Identify the blood parasite species.
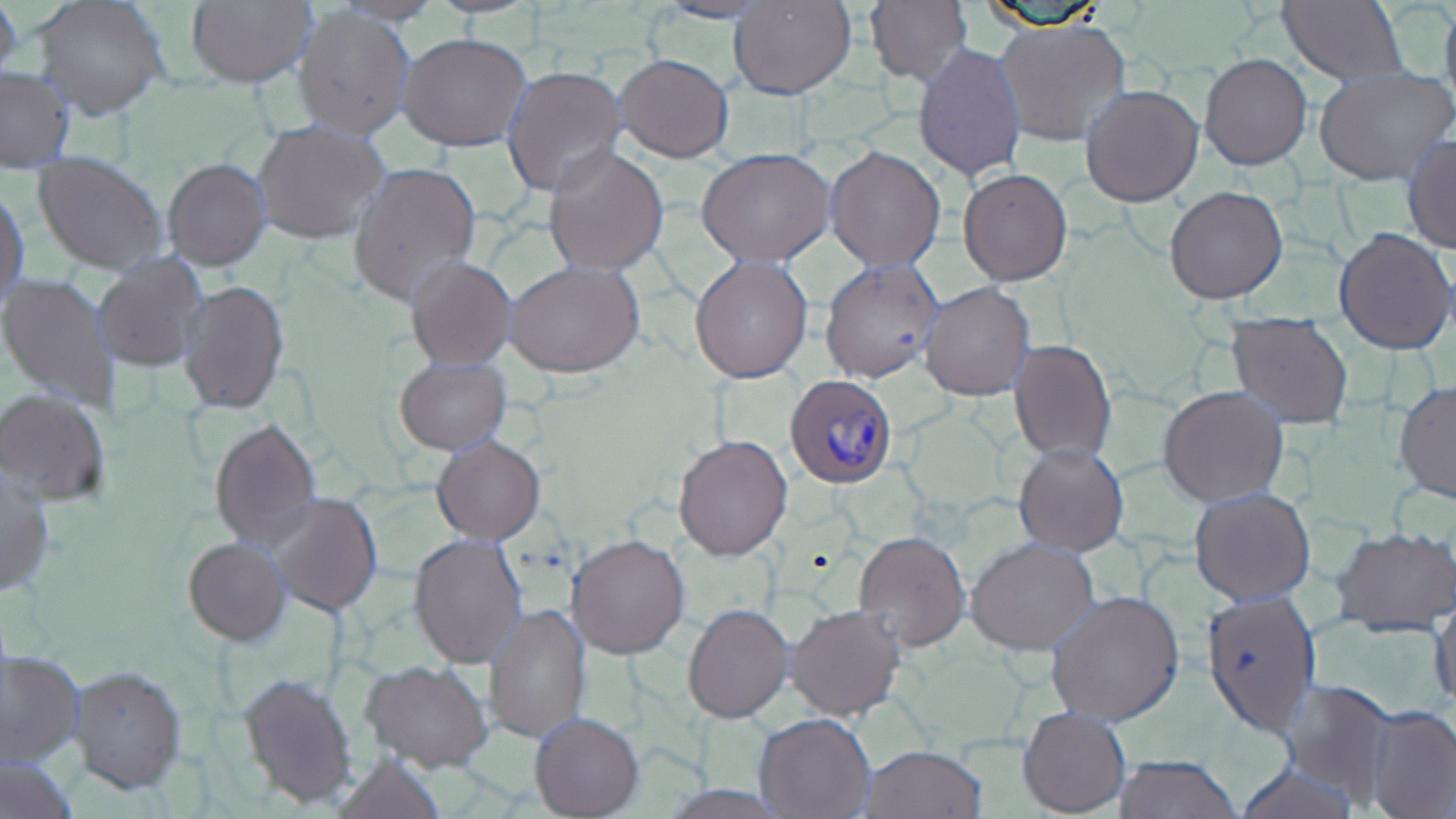
Plasmodium ovale.

Approximate bounding boxes as named x1/y1/x2/y2 corners in pixels. Plasmodium ovale-infected red blood cell locations: (x1=785, y1=373, x2=899, y2=486). Uninfected red blood cell locations: (x1=0, y1=0, x2=23, y2=85), (x1=33, y1=0, x2=170, y2=120), (x1=185, y1=0, x2=314, y2=89), (x1=729, y1=0, x2=856, y2=99), (x1=866, y1=0, x2=973, y2=88), (x1=1278, y1=0, x2=1407, y2=87), (x1=1439, y1=0, x2=1456, y2=117), (x1=651, y1=1, x2=779, y2=23), (x1=293, y1=5, x2=415, y2=139), (x1=994, y1=18, x2=1131, y2=146), (x1=398, y1=32, x2=533, y2=152), (x1=913, y1=42, x2=1027, y2=183), (x1=615, y1=53, x2=733, y2=163), (x1=1198, y1=53, x2=1312, y2=170), (x1=501, y1=66, x2=628, y2=198), (x1=1314, y1=67, x2=1454, y2=185), (x1=0, y1=68, x2=73, y2=173), (x1=1081, y1=84, x2=1203, y2=207), (x1=253, y1=120, x2=391, y2=246), (x1=1403, y1=135, x2=1456, y2=253), (x1=542, y1=145, x2=670, y2=278), (x1=825, y1=146, x2=945, y2=269), (x1=696, y1=147, x2=834, y2=266), (x1=32, y1=154, x2=168, y2=276), (x1=163, y1=159, x2=270, y2=270), (x1=349, y1=161, x2=482, y2=306), (x1=958, y1=169, x2=1072, y2=285), (x1=1164, y1=186, x2=1288, y2=303), (x1=1, y1=187, x2=28, y2=313), (x1=1333, y1=226, x2=1455, y2=355), (x1=93, y1=253, x2=210, y2=373), (x1=689, y1=253, x2=813, y2=383), (x1=405, y1=255, x2=517, y2=370), (x1=820, y1=258, x2=942, y2=383), (x1=505, y1=260, x2=646, y2=378), (x1=0, y1=272, x2=121, y2=412), (x1=178, y1=279, x2=289, y2=415), (x1=920, y1=282, x2=1036, y2=400), (x1=1226, y1=315, x2=1352, y2=428), (x1=1010, y1=339, x2=1116, y2=463), (x1=409, y1=355, x2=523, y2=541), (x1=395, y1=356, x2=511, y2=454), (x1=1394, y1=381, x2=1456, y2=502), (x1=1159, y1=386, x2=1289, y2=505), (x1=0, y1=388, x2=112, y2=505), (x1=208, y1=416, x2=321, y2=550), (x1=673, y1=433, x2=792, y2=561), (x1=432, y1=435, x2=545, y2=544), (x1=1013, y1=443, x2=1128, y2=555), (x1=0, y1=466, x2=54, y2=598), (x1=1192, y1=486, x2=1314, y2=604), (x1=265, y1=492, x2=383, y2=615), (x1=1332, y1=526, x2=1456, y2=636), (x1=855, y1=529, x2=970, y2=651), (x1=409, y1=533, x2=527, y2=670), (x1=567, y1=534, x2=690, y2=659), (x1=183, y1=537, x2=290, y2=644), (x1=966, y1=537, x2=1099, y2=654), (x1=1046, y1=589, x2=1187, y2=725), (x1=1199, y1=591, x2=1321, y2=735), (x1=1433, y1=595, x2=1455, y2=710), (x1=484, y1=603, x2=592, y2=745), (x1=683, y1=603, x2=793, y2=721), (x1=786, y1=604, x2=905, y2=719), (x1=1, y1=649, x2=84, y2=766), (x1=362, y1=658, x2=493, y2=771), (x1=69, y1=666, x2=188, y2=793), (x1=239, y1=672, x2=358, y2=809), (x1=1279, y1=679, x2=1394, y2=800), (x1=1362, y1=705, x2=1456, y2=817), (x1=1017, y1=706, x2=1131, y2=816), (x1=530, y1=712, x2=643, y2=818), (x1=755, y1=712, x2=874, y2=818), (x1=863, y1=745, x2=985, y2=818), (x1=329, y1=752, x2=445, y2=817), (x1=0, y1=754, x2=79, y2=819), (x1=1112, y1=755, x2=1244, y2=818), (x1=1233, y1=761, x2=1362, y2=819). Image is 1456×819 pixels. Captured at 1000x magnification. Thin blood film. Single field of view. Optical microscopy. May-Grünwald-Giemsa stain.